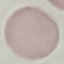 Malaria status: uninfected. Giemsa-stained preparation. Automatically extracted cell patch, resized to 64 × 64 pixels. Thin blood film. Photographed with a smartphone camera at the microscope eyepiece.